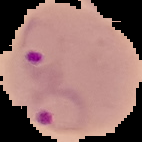
Summary:
  - Image size: 142×142 pixels
  - Malaria status: parasitized
  - Preparation: thin blood smear
  - Image type: segmented cell region on a black background